Report the malaria status of this cell.
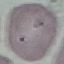

Uninfected.

Summary:
  - Image type: automatically extracted cell patch, resized to 64 × 64 pixels
  - Stain: Giemsa
  - Capture: smartphone through the microscope eyepiece
  - Preparation: thin blood smear